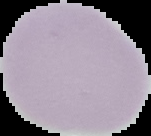
Summary:
  - Malaria status: uninfected
  - Image size: 151×136 pixels
  - Image type: segmented cell region on a black background
  - Preparation: thin blood smear